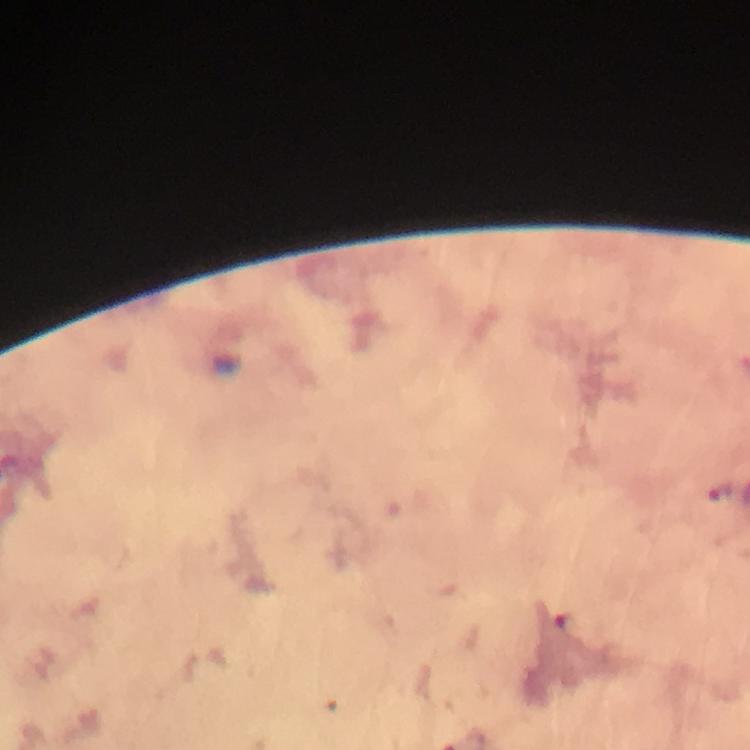

Approximate centers as {x, y} in pixels.
Summary:
  - Plasmodium parasite locations: {718, 490}
  - Magnification: 100x
  - Cropped from: one field of view
  - Context: from a malaria diagnostic workup
  - Preparation: thick blood film
  - Immersion oil: used
  - Stain: Giemsa
  - Image size: 750×750 pixels
  - Capture: smartphone photograph through a microscope